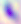
Photomicrograph. Toxoplasma gondii is shown. 400x magnification.